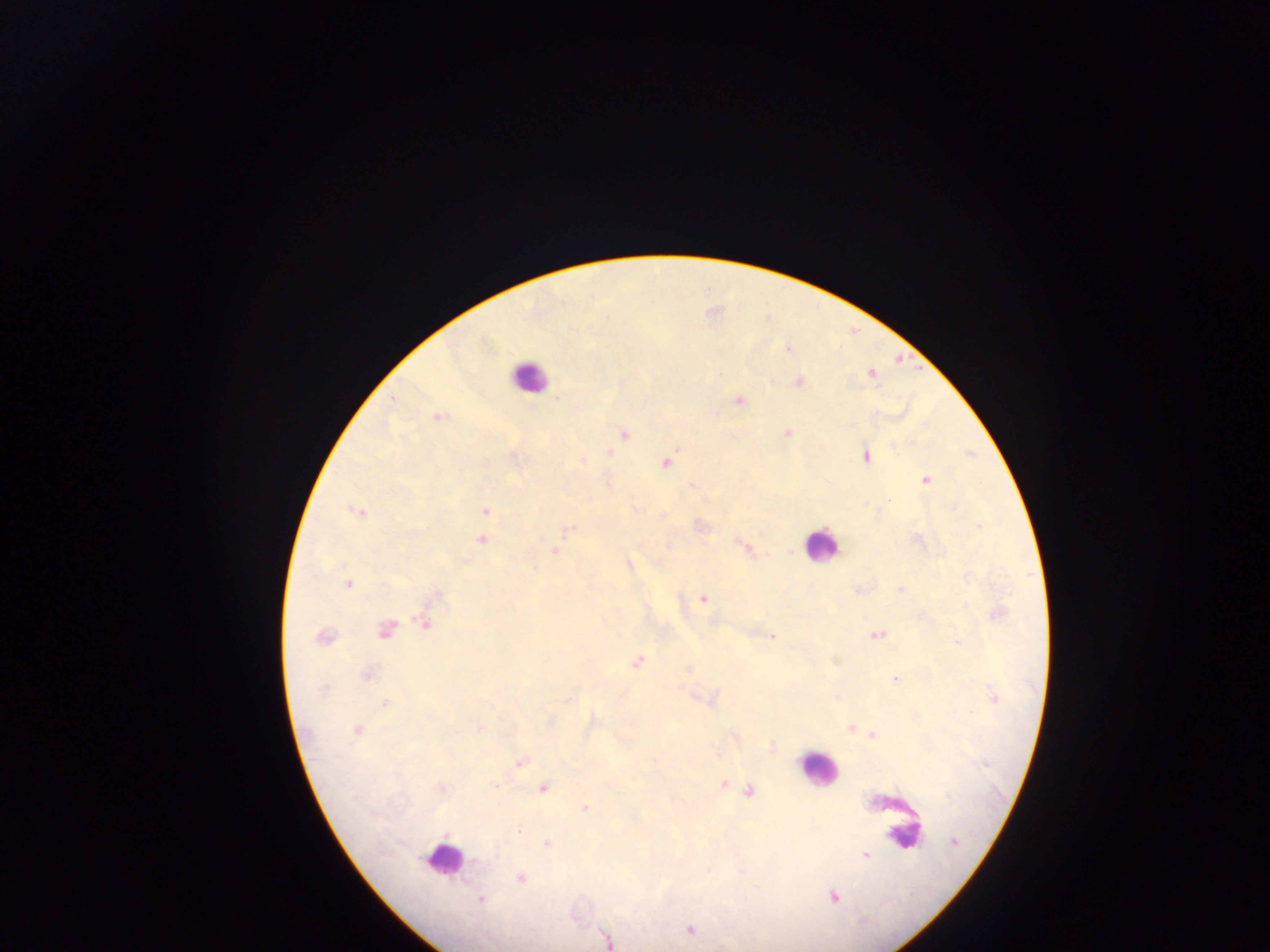

Approximate centers as {x, y} in pixels.
Summary:
  - Leukocyte locations: {528, 376}, {820, 545}, {817, 769}, {891, 815}, {902, 831}, {442, 859}
  - Malaria parasite locations: {788, 348}, {870, 373}, {797, 382}, {392, 400}, {738, 400}, {438, 416}, {788, 432}, {623, 433}, {608, 452}, {866, 455}, {581, 460}, {665, 462}, {925, 479}, {607, 483}, {693, 486}, {485, 510}, {358, 511}, {699, 526}, {979, 526}, {566, 529}, {481, 539}, {740, 543}, {746, 547}, {554, 550}, {628, 565}, {347, 584}, {900, 589}, {437, 595}, {703, 598}, {998, 613}, {425, 621}, {384, 629}, {877, 635}, {325, 637}, {771, 637}, {956, 642}, {637, 662}, {687, 668}, {367, 675}, {894, 679}, {323, 689}, {568, 699}, {711, 699}, {994, 699}, {385, 703}, {591, 721}, {548, 722}, {850, 727}, {480, 728}, {357, 730}, {872, 734}, {771, 746}, {655, 758}, {519, 762}, {987, 765}, {724, 783}, {543, 788}, {740, 788}, {440, 789}, {748, 791}, {585, 809}, {954, 842}, {545, 843}, {865, 854}, {520, 877}, {834, 897}, {479, 900}, {688, 929}, {607, 939}
  - Preparation: thick blood film
  - Country: Ghana
  - Image size: 1270×952 pixels
  - Capture: mobile-phone photograph through a microscope
  - Field of view: single